Name the parasite shown.
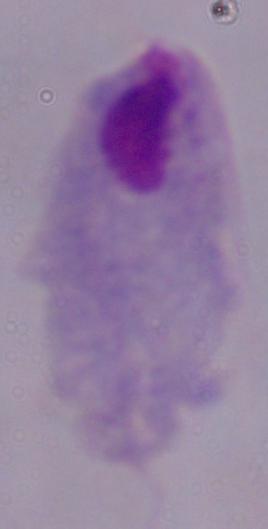
A trichomonad.

magnification = 1000x
modality = micrograph